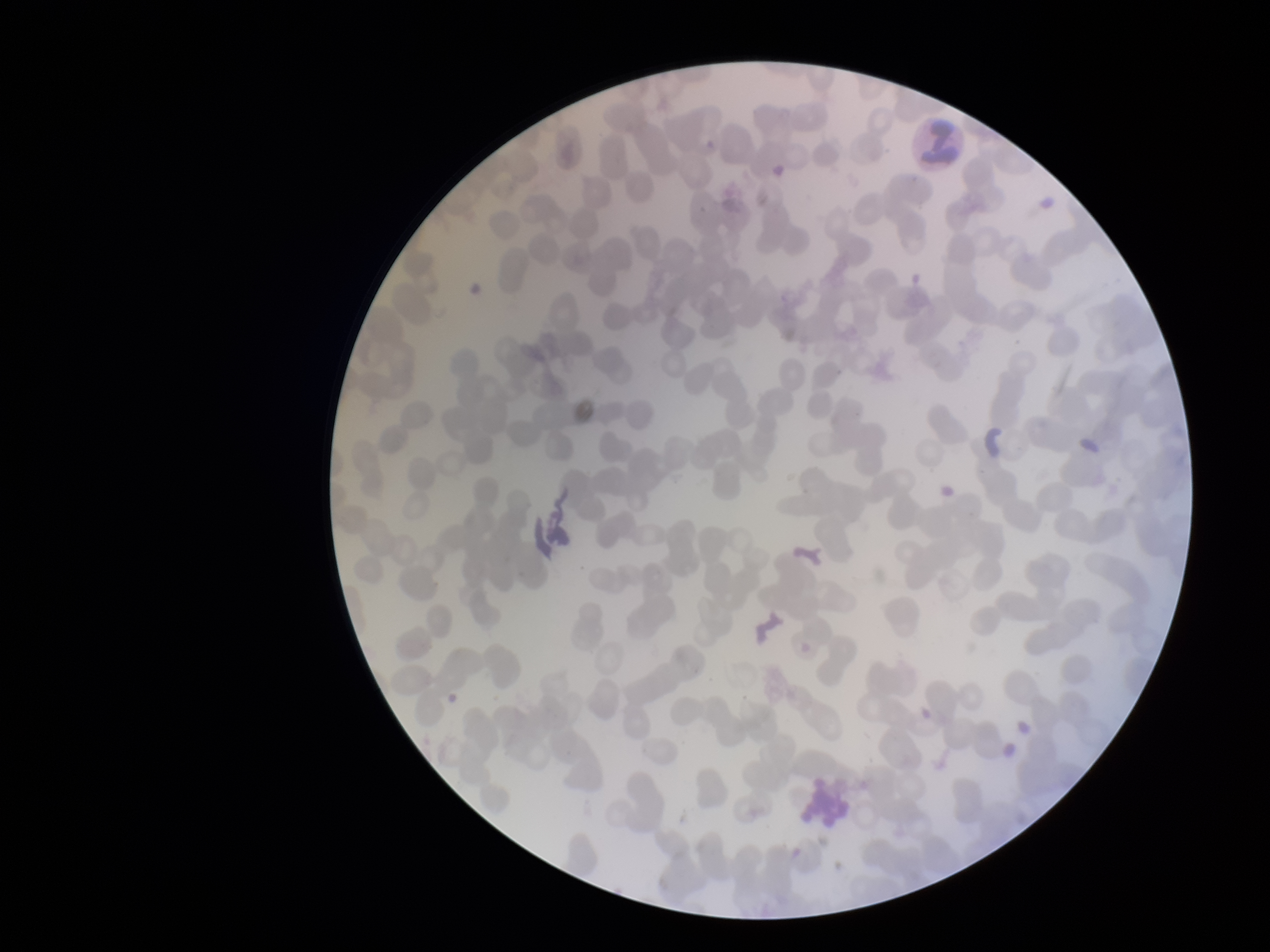
{
  "preparation": "thin blood smear",
  "parasitized_red_blood_cells": "none seen",
  "stain": "Giemsa",
  "image_size": "1270×952 pixels",
  "field_of_view": "one from this slide",
  "red_blood_cell_count": 261,
  "patient_malaria_status": "negative",
  "capture": "smartphone photograph through the microscope eyepiece",
  "parasitized_red_blood_cell_count": 0
}